State the blood parasite species.
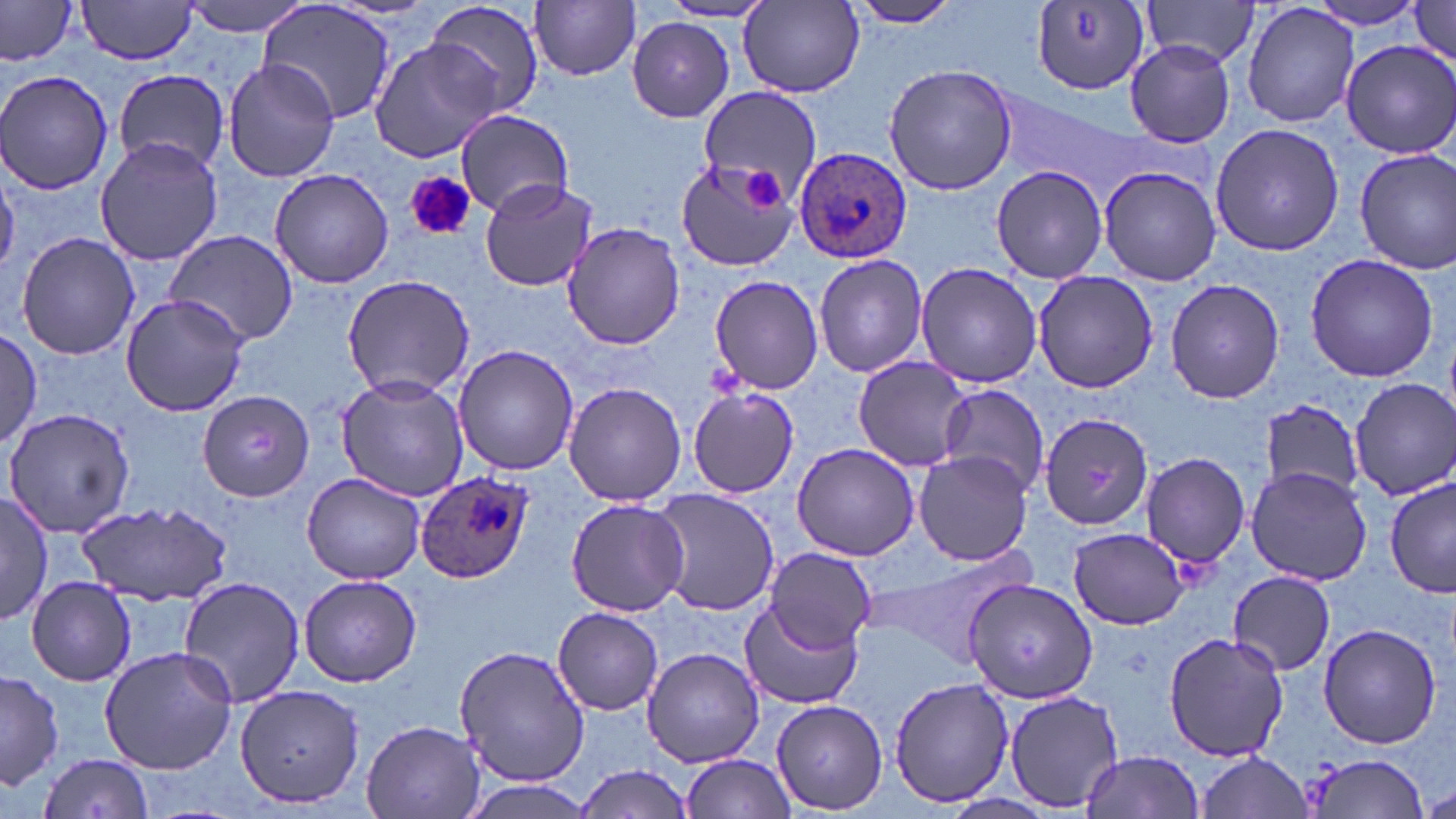
Plasmodium ovale.

Summary:
  - Coordinate format: approximate bounding boxes as [x1, y1, x2, y2] in pixels
  - Plasmodium ovale-infected red blood cell locations: [793, 148, 912, 266], [417, 471, 533, 583]
  - Uninfected red blood cell locations: [75, 0, 200, 65], [181, 0, 315, 38], [843, 0, 963, 27], [1142, 0, 1266, 72], [1301, 0, 1433, 30], [423, 1, 546, 117], [531, 1, 642, 81], [1407, 1, 1455, 67], [1029, 2, 1150, 94], [1241, 2, 1359, 127], [256, 3, 397, 125], [659, 3, 775, 23], [738, 3, 866, 98], [0, 4, 76, 67], [626, 17, 735, 122], [371, 39, 503, 163], [1123, 40, 1238, 148], [1340, 40, 1456, 162], [223, 59, 338, 183], [884, 64, 1019, 195], [0, 70, 118, 193], [115, 70, 228, 173], [697, 85, 821, 201], [999, 93, 1143, 196], [455, 109, 575, 217], [1210, 123, 1347, 257], [94, 135, 222, 265], [1355, 148, 1456, 275], [675, 155, 803, 274], [0, 160, 21, 273], [989, 164, 1108, 282], [1096, 166, 1222, 285], [269, 168, 394, 288], [479, 177, 599, 294], [561, 224, 688, 350], [165, 229, 298, 346], [15, 231, 141, 360], [813, 253, 928, 378], [1304, 253, 1439, 383], [915, 261, 1042, 388], [1031, 270, 1160, 393], [341, 273, 476, 398], [709, 276, 825, 394], [1166, 278, 1285, 404], [119, 294, 250, 417], [0, 330, 43, 449], [452, 344, 581, 475], [851, 355, 973, 473], [336, 376, 468, 500], [1350, 379, 1456, 499], [563, 382, 687, 507], [935, 383, 1049, 493], [686, 387, 799, 497], [196, 391, 317, 502], [1259, 400, 1367, 498], [4, 407, 135, 537], [1056, 413, 1206, 545], [792, 443, 919, 561], [913, 449, 1033, 565], [1139, 453, 1249, 570], [1246, 465, 1372, 586], [302, 472, 427, 584], [1385, 477, 1455, 600], [651, 489, 778, 617], [0, 492, 51, 626], [564, 497, 691, 617], [79, 501, 233, 602], [1067, 526, 1192, 630], [869, 545, 1036, 664], [763, 546, 877, 655], [1228, 570, 1336, 675], [298, 573, 422, 687], [25, 576, 136, 686], [175, 576, 307, 708], [965, 577, 1099, 705], [738, 599, 862, 710], [553, 607, 664, 715], [1317, 623, 1442, 749], [1162, 629, 1287, 763], [454, 644, 591, 787], [99, 645, 237, 775], [641, 646, 766, 769], [0, 669, 64, 790], [889, 676, 1015, 808], [235, 682, 367, 808], [1005, 689, 1125, 812], [771, 698, 887, 813], [360, 719, 486, 819], [1195, 750, 1313, 819], [1080, 751, 1207, 818], [680, 753, 797, 818], [35, 754, 157, 819], [1303, 755, 1431, 817], [575, 764, 695, 817], [459, 782, 598, 817], [1424, 783, 1456, 817]
  - Platelet locations: [740, 168, 788, 211], [404, 170, 475, 241]
  - Stain: May-Grünwald-Giemsa
  - Preparation: thin blood film
  - Magnification: 1000x
  - Field of view: one of a larger specimen
  - Modality: optical microscopy
  - Image size: 1456×819 pixels